Identify the parasite.
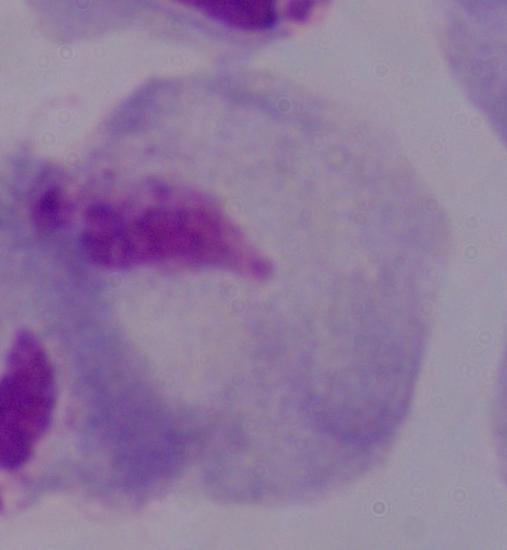
This is a trichomonad.

Photomicrograph. Captured at 1000x magnification.